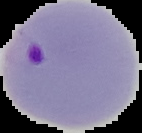
Summary:
  - Image type: cell region segmented out of the field of view; surrounding area masked to black
  - Result: Plasmodium parasites detected
  - Image size: 142×133 pixels
  - Preparation: thin blood film